Report the malaria status of this cell.
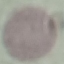

Uninfected.

Summary:
  - Stain: Giemsa
  - Image type: automatically extracted cell patch, resized to 64 × 64 pixels
  - Preparation: thin blood smear
  - Capture: smartphone camera at the microscope eyepiece